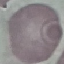

malaria status = uninfected
stain = Giemsa
image type = automatically extracted cell patch, resized to 64 × 64 pixels
capture = smartphone camera at the microscope eyepiece
preparation = thin smear